Assess this cell for malaria.
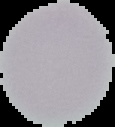

It is uninfected.

preparation = thin blood film
image size = 115×127 pixels
image type = segmented cell region with the area outside set to black